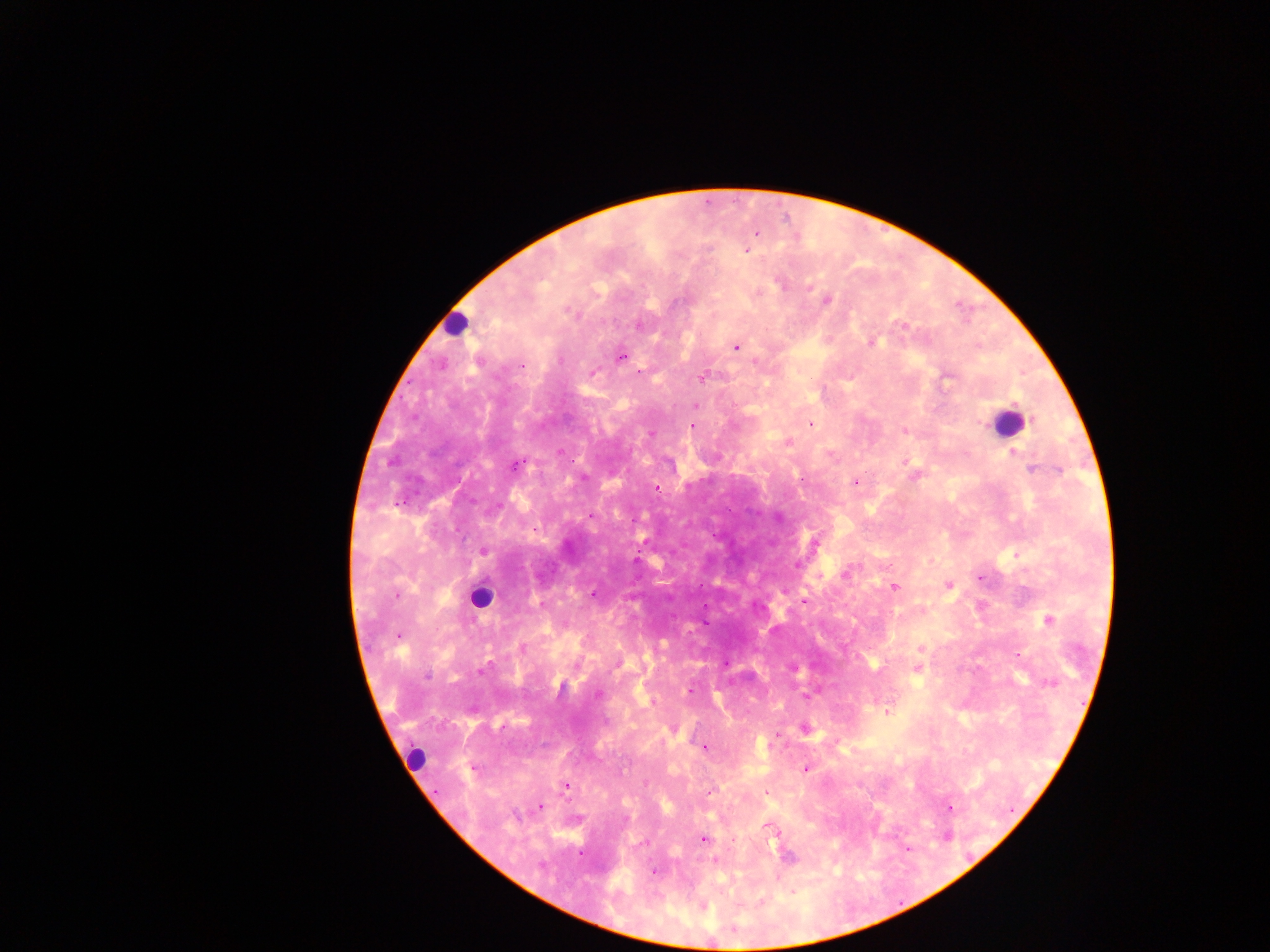
Approximate centers as (x, y) in pixels.
Summary:
  - Plasmodium parasite locations: (756, 234), (747, 251), (780, 283), (810, 286), (827, 300), (568, 311), (903, 325), (639, 326), (870, 342), (736, 348), (621, 357), (560, 360), (442, 364), (521, 366), (639, 371), (592, 373), (703, 378), (696, 405), (810, 424), (693, 425), (904, 431), (651, 434), (1014, 452), (906, 463), (517, 464), (1033, 470), (1059, 471), (855, 482), (656, 488), (590, 516), (534, 529), (815, 544), (483, 551), (796, 566), (846, 572), (981, 578), (949, 586), (894, 587), (592, 594), (397, 596), (805, 602), (1048, 621), (399, 636), (523, 648), (921, 649), (1020, 655), (917, 669), (481, 672), (427, 676), (1051, 683), (689, 690), (598, 694), (808, 696), (887, 712), (805, 729), (776, 735), (704, 748), (806, 768), (474, 769), (566, 787), (709, 792), (765, 792), (540, 807), (951, 808), (769, 828), (704, 839), (581, 854), (788, 857), (715, 860), (540, 865), (654, 872), (703, 907)
  - Leukocyte locations: (454, 324), (1007, 424), (480, 598), (415, 757)
  - Preparation: thick blood film
  - Capture: mobile-phone photograph through a microscope
  - Image size: 1270×952 pixels
  - Field of view: single
  - Country: Ghana